Assess the morphology of the red blood cells.
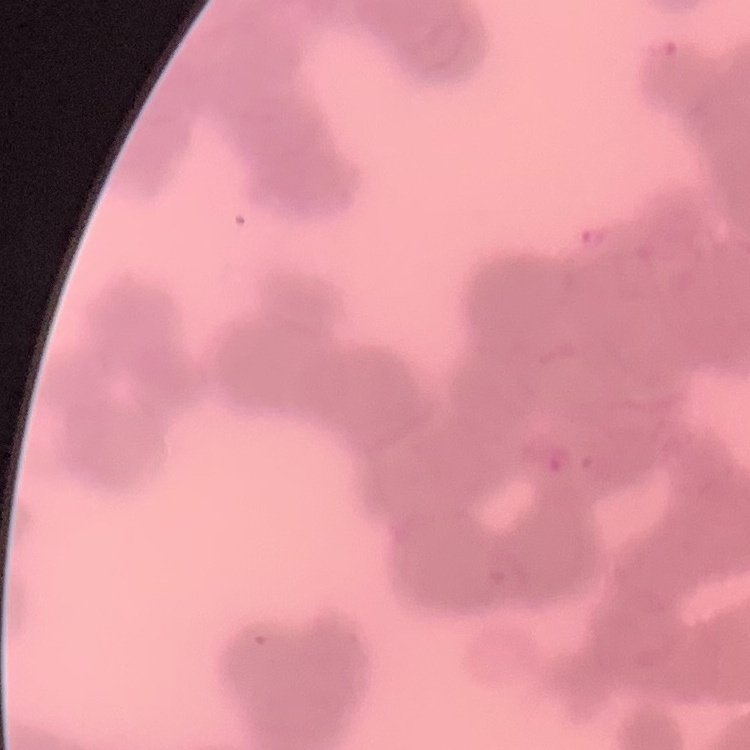

Rouleaux formation.

Summary:
  - Image type: one tile cut from a larger photomicrograph
  - Preparation: thin peripheral smear
  - Stain: Field's or Giemsa